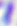
Summary:
  - Modality: photomicrograph
  - Identification: Toxoplasma gondii
  - Magnification: 400x